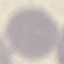

malaria status = uninfected
image type = cell patch, automatically extracted from a larger field of view and resized to 64 × 64 pixels
preparation = thin blood film
capture = smartphone camera at the microscope eyepiece
stain = Giemsa